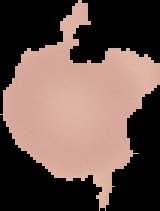 Segmented cell region on a black background. From a thin blood film. Image is 160×211 pixels. Result: negative for Plasmodium parasites.